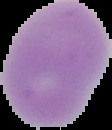
{
  "preparation": "thin blood smear",
  "image_type": "segmented cell region with the area outside set to black",
  "image_size": "112×130 pixels",
  "malaria_status": "uninfected"
}